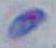

modality = micrograph
identification = Toxoplasma gondii
magnification = 1000x